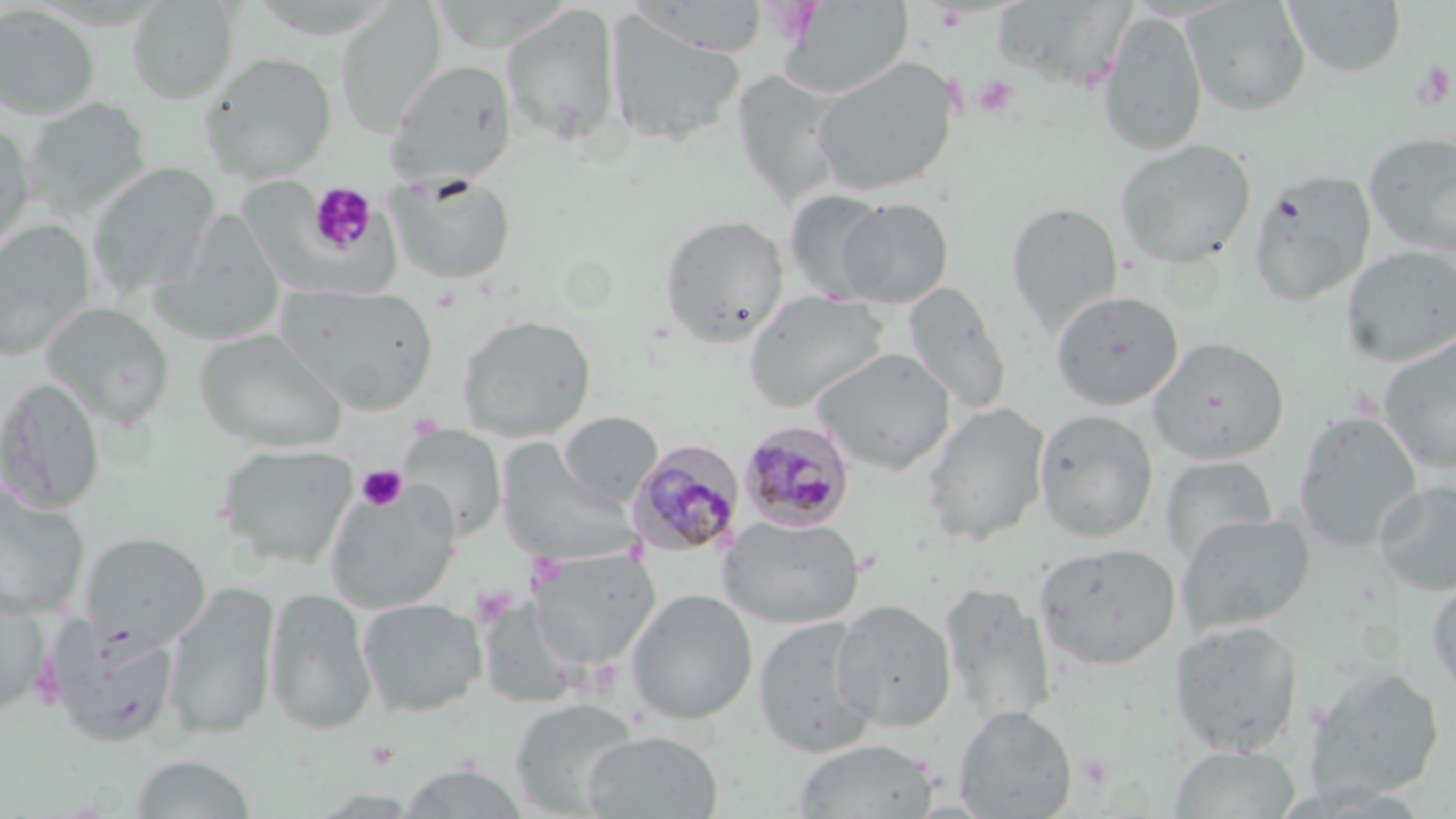

slide-level diagnosis = Plasmodium malariae
image size = 1456×819 pixels
magnification = 1000x
stain = May-Grünwald-Giemsa
field of view = single
uninfected red blood cell locations = approximate bounding boxes as (x1,y1)-(x2,y2) corner pairs in pixels: (245,0)-(400,40), (428,0)-(574,53), (1183,0)-(1311,116), (1284,0)-(1407,77), (127,1)-(239,104), (779,1)-(914,99), (335,3)-(446,136), (501,4)-(621,146), (0,5)-(100,119), (604,9)-(746,148), (1097,9)-(1208,156), (199,52)-(338,183), (812,57)-(958,196), (387,60)-(517,186), (729,71)-(848,211), (22,97)-(152,219), (0,123)-(37,255), (1364,132)-(1456,257), (1115,138)-(1257,269), (86,162)-(220,298), (1249,169)-(1376,307), (384,173)-(518,285), (784,189)-(891,302), (834,197)-(955,307), (1006,201)-(1122,335), (659,213)-(789,346), (150,215)-(286,344), (0,220)-(96,360), (1341,244)-(1456,366), (276,283)-(438,412), (903,284)-(1013,415), (744,290)-(886,412), (1051,290)-(1184,411), (42,302)-(174,426), (457,314)-(596,440), (194,328)-(346,453), (1377,334)-(1456,473), (1148,337)-(1289,464), (811,347)-(956,474), (0,377)-(105,514), (921,402)-(1051,545), (1034,408)-(1159,542), (1293,410)-(1422,553), (558,411)-(661,506), (398,424)-(507,540), (495,439)-(639,565), (216,442)-(358,568), (1161,455)-(1278,563), (1375,479)-(1456,596), (0,483)-(89,618), (324,484)-(460,613), (1177,511)-(1315,636), (719,515)-(864,628), (81,532)-(210,648), (1035,542)-(1181,669), (527,547)-(661,668), (1427,575)-(1456,700), (940,581)-(1057,727), (163,582)-(281,739), (263,586)-(378,735), (0,587)-(50,715), (627,588)-(758,724), (357,597)-(486,718), (831,598)-(957,732), (753,615)-(879,757), (45,618)-(181,746), (1171,620)-(1304,756), (1306,665)-(1444,799), (509,698)-(640,816), (954,705)-(1077,818), (581,729)-(723,819), (790,739)-(941,819), (1170,745)-(1300,818), (127,753)-(257,818), (398,762)-(530,818)
modality = light microscopy
platelet locations = approximate bounding boxes as (x1,y1)-(x2,y2) corner pairs in pixels: (1411,60)-(1454,111), (973,75)-(1018,117), (308,183)-(377,255), (356,464)-(407,511), (471,585)-(518,625)
Plasmodium malariae-infected red blood cell locations = approximate bounding boxes as (x1,y1)-(x2,y2) corner pairs in pixels: (738,419)-(856,531), (625,439)-(746,558)
preparation = thin blood film